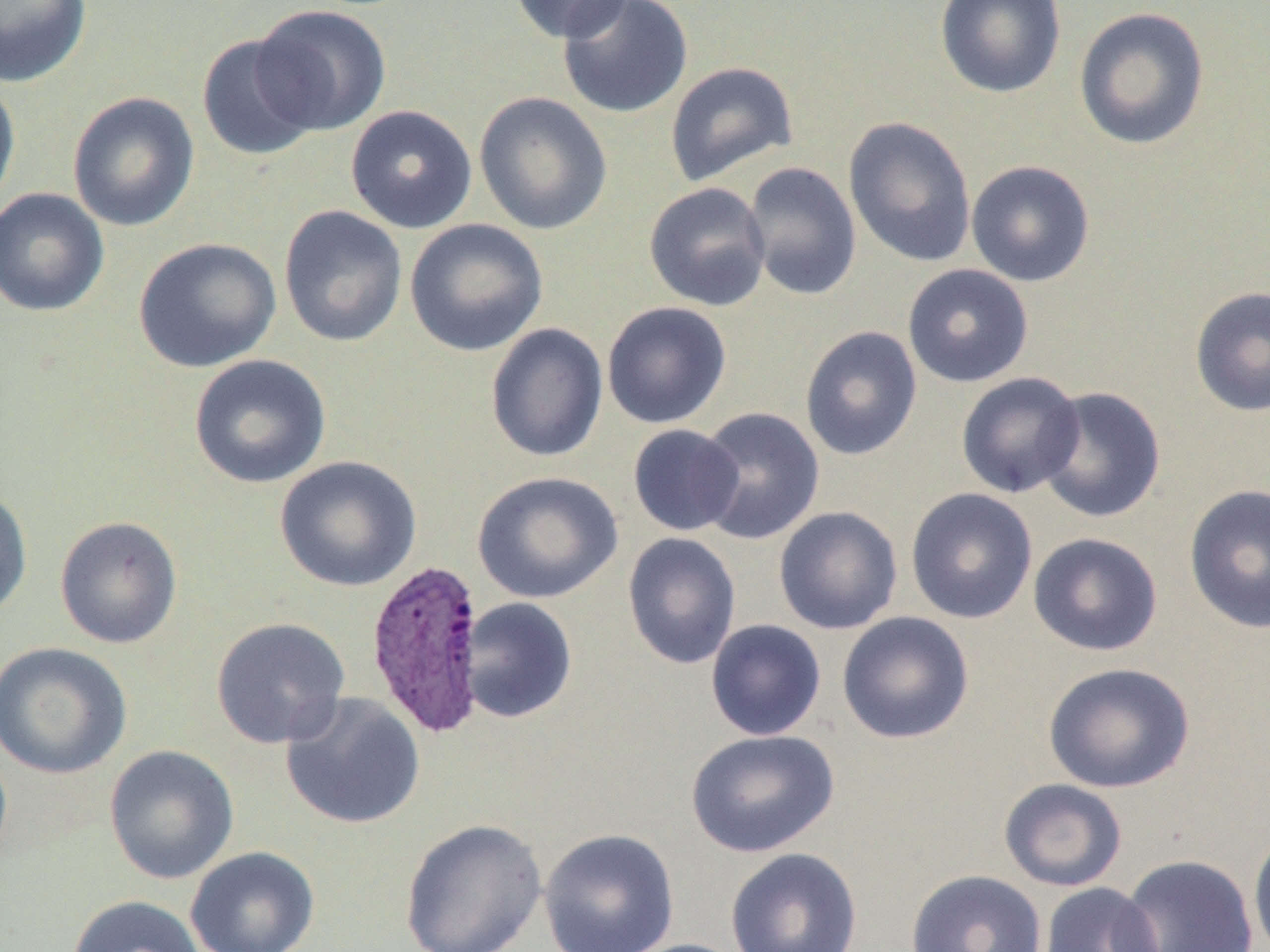

Summary:
  - Coordinate format: approximate bounding boxes as (x1, y1, x2, y2) in pixels
  - Uninfected red blood cell locations: (0, 0, 93, 88), (508, 0, 635, 43), (557, 0, 693, 119), (934, 0, 1066, 99), (252, 4, 392, 136), (1073, 6, 1210, 151), (195, 34, 322, 161), (664, 61, 798, 187), (0, 78, 21, 214), (67, 91, 200, 232), (474, 91, 613, 235), (345, 104, 477, 234), (843, 116, 977, 268), (966, 160, 1095, 287), (743, 161, 862, 300), (644, 182, 772, 312), (0, 187, 110, 318), (278, 204, 408, 347), (404, 219, 549, 357), (133, 236, 281, 373), (902, 263, 1034, 388), (1189, 285, 1270, 418), (601, 301, 732, 429), (485, 322, 609, 463), (799, 325, 923, 461), (188, 354, 331, 489), (956, 371, 1086, 498), (1036, 386, 1167, 524), (694, 406, 825, 545), (627, 424, 744, 536), (274, 455, 421, 592), (472, 470, 623, 604), (1183, 483, 1269, 635), (0, 485, 33, 620), (905, 488, 1038, 624), (773, 505, 903, 636), (54, 516, 183, 649), (622, 531, 741, 670), (1027, 531, 1163, 657), (459, 597, 578, 723), (836, 611, 975, 744), (210, 617, 350, 749), (705, 619, 826, 741), (0, 641, 133, 779), (1042, 661, 1195, 793), (280, 692, 427, 830), (685, 728, 840, 858), (103, 744, 239, 884), (998, 778, 1128, 892), (398, 817, 548, 952), (538, 828, 680, 952), (1248, 828, 1270, 952), (185, 846, 320, 952), (725, 847, 863, 952), (1118, 853, 1259, 952), (905, 869, 1047, 952), (1038, 883, 1164, 952), (66, 894, 206, 952), (616, 938, 751, 952)
  - Plasmodium vivax-infected red blood cell locations: (364, 557, 488, 738)
  - Slide-level diagnosis: Plasmodium vivax
  - Field of view: one of a larger specimen
  - Magnification: 1000x
  - Image size: 1270×952 pixels
  - Modality: light microscopy
  - Preparation: thin blood smear